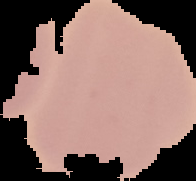 From a thin blood smear. Malaria status: uninfected. Segmented cell region on a black background. Image is 196×181 pixels.